Describe the morphology of the erythrocytes.
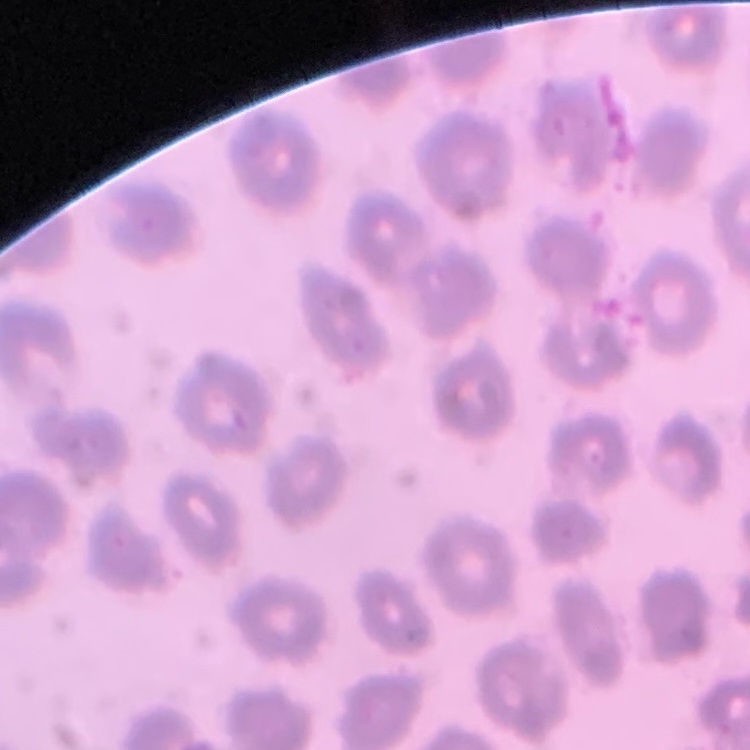
No rouleaux formation.

preparation = thin blood film
stain = Field's or Giemsa
image type = one tile cut from a larger photomicrograph